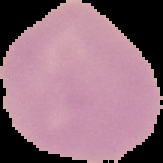

image size = 163×163 pixels
preparation = thin blood smear
image type = segmented cell region with the area outside set to black
result = negative for Plasmodium parasites